Give the position of every Plasmodium parasite.
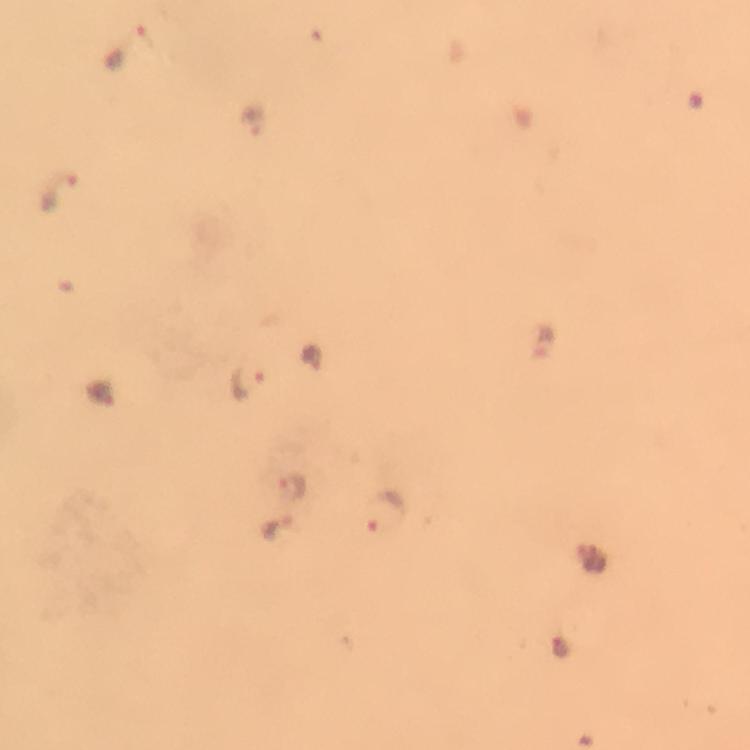

Approximate object centers, in pixels from the top-left corner.
Plasmodium parasites: (x=126, y=46), (x=255, y=122), (x=59, y=194), (x=541, y=346), (x=246, y=382), (x=293, y=486), (x=384, y=509), (x=276, y=528), (x=590, y=559), (x=559, y=648).

{
  "immersion_oil": "applied",
  "preparation": "thick smear",
  "cropped_from": "a single field of view",
  "context": "from a diagnostic examination for malaria",
  "capture": "smartphone photograph through a microscope",
  "image_size": "750×750 pixels",
  "magnification": "100x",
  "stain": "Giemsa"
}